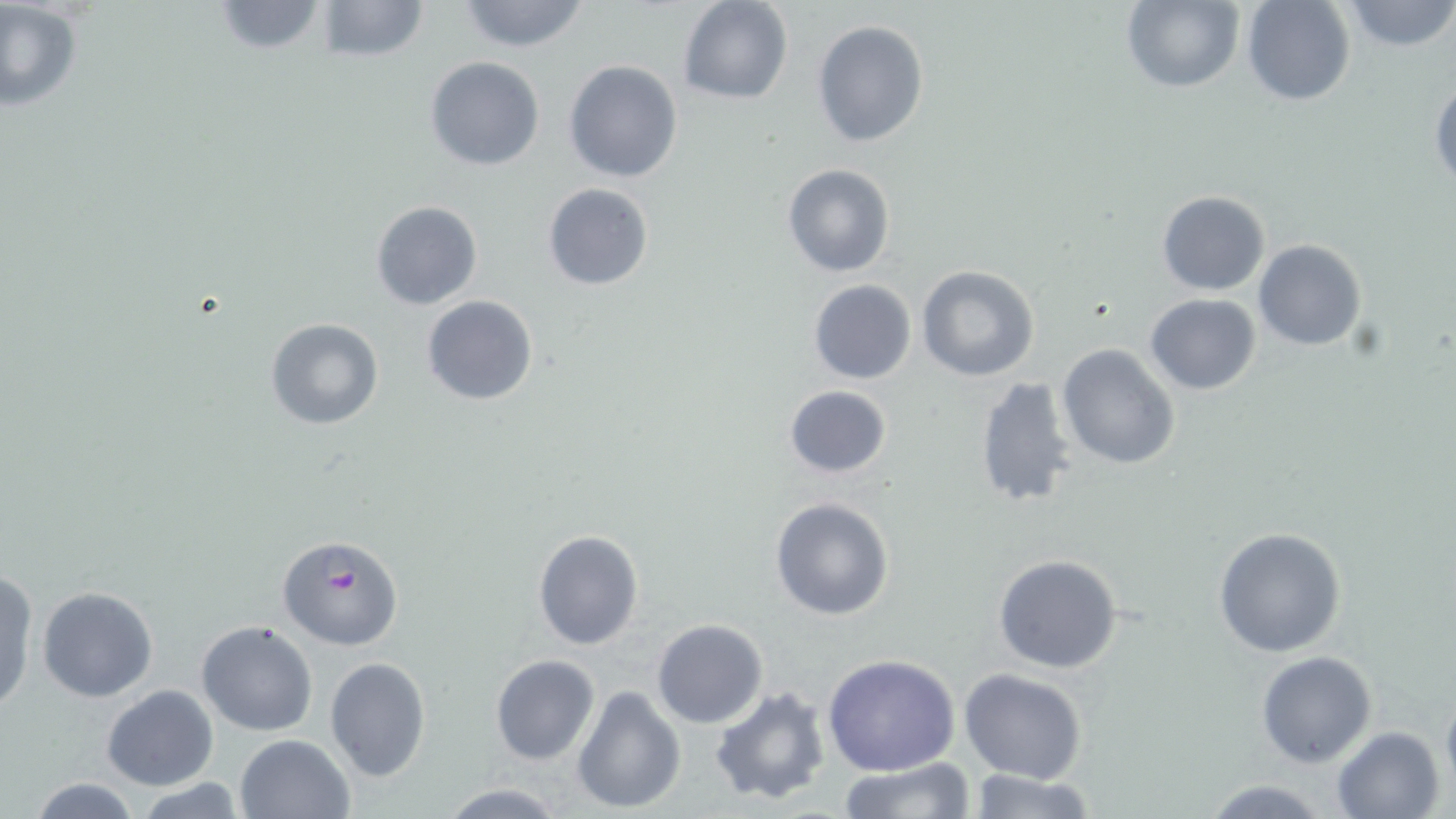

Summary:
  - Coordinate format: approximate bounding boxes as (x1,y1)-(x2,y2) corner pairs in pixels
  - Plasmodium falciparum-infected red blood cell locations: (279,534)-(405,652)
  - Uninfected red blood cell locations: (207,0)-(334,55), (311,0)-(431,64), (454,0)-(593,53), (678,0)-(793,105), (1119,0)-(1244,92), (1240,0)-(1356,106), (1338,0)-(1456,52), (0,3)-(82,113), (811,20)-(929,148), (425,57)-(544,170), (563,60)-(683,183), (1429,76)-(1456,189), (782,164)-(895,278), (542,183)-(654,291), (1157,191)-(1270,295), (369,199)-(483,311), (1253,240)-(1367,351), (916,266)-(1041,382), (806,280)-(916,385), (1144,293)-(1261,395), (421,295)-(540,406), (265,318)-(384,429), (1057,344)-(1180,469), (973,374)-(1082,512), (784,385)-(892,479), (769,496)-(895,621), (1211,526)-(1347,659), (532,528)-(644,649), (993,553)-(1124,673), (0,566)-(36,712), (37,585)-(159,702), (653,619)-(768,728), (197,620)-(317,736), (1256,650)-(1377,768), (823,652)-(961,776), (490,654)-(600,766), (325,656)-(431,783), (959,669)-(1088,785), (100,684)-(218,791), (572,685)-(685,814), (1441,685)-(1456,802), (709,686)-(834,807), (1332,726)-(1447,818), (234,732)-(356,819), (835,759)-(977,818), (965,768)-(1095,819), (25,777)-(145,818), (1200,778)-(1330,817), (137,779)-(245,817), (435,781)-(569,817)
  - Slide-level diagnosis: Plasmodium falciparum
  - Image size: 1456×819 pixels
  - Modality: light microscopy
  - Magnification: 1000x
  - Preparation: thin blood smear
  - Field of view: one of a larger specimen
  - Stain: May-Grünwald-Giemsa